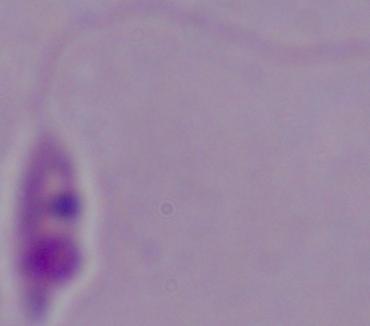
modality: micrograph
identification: Leishmania
magnification: 1000x